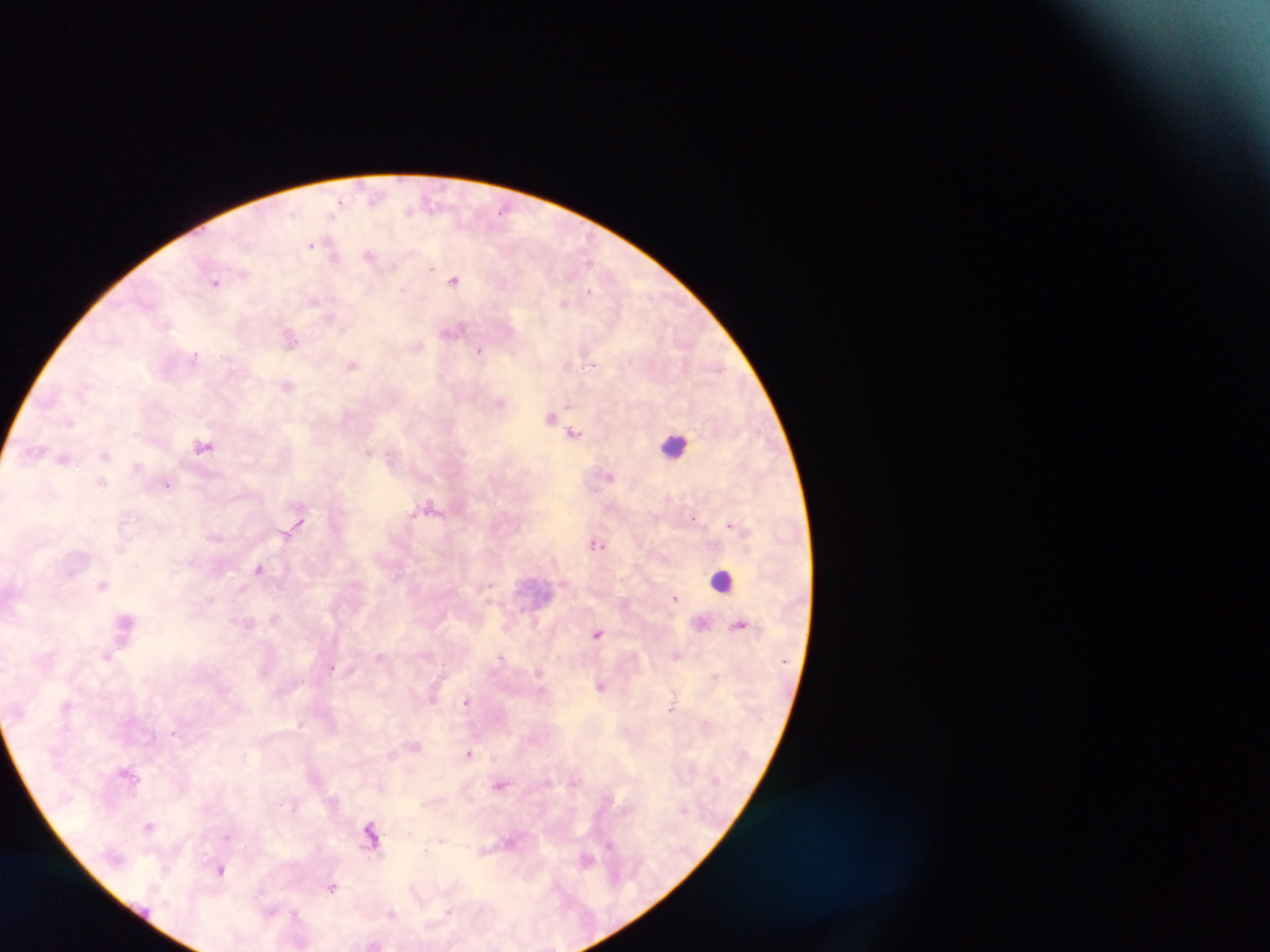
Plasmodium parasite locations = approximate centers as (x, y) in pixels: (295, 210), (410, 210), (501, 210), (330, 218), (311, 245), (370, 255), (333, 257), (588, 262), (431, 269), (453, 280), (216, 282), (402, 288), (589, 289), (564, 303), (329, 320), (290, 338), (419, 345), (481, 350), (195, 353), (567, 365), (593, 365), (351, 366), (287, 385), (499, 402), (568, 403), (551, 417), (575, 433), (202, 447), (369, 450), (105, 455), (391, 457), (139, 465), (610, 477), (101, 482), (168, 484), (432, 504), (302, 517), (695, 519), (731, 526), (286, 532), (597, 544), (258, 567), (103, 585), (488, 586), (677, 598), (273, 618), (125, 623), (740, 624), (598, 634), (380, 655), (675, 655), (107, 656), (502, 657), (332, 670), (600, 686), (433, 698), (467, 701), (67, 704), (672, 708), (302, 724), (175, 734), (414, 744), (469, 753), (126, 772), (574, 780), (501, 784), (334, 801), (294, 809), (369, 824), (148, 826), (370, 830), (228, 835), (441, 839), (610, 843), (371, 845), (425, 851), (151, 852), (587, 859), (219, 870), (331, 888), (416, 889), (270, 910), (449, 910), (296, 912), (391, 914)
image size = 1270×952 pixels
capture = mobile-phone photograph through a microscope
field of view = single
preparation = thick blood film
country = Ghana
leukocyte locations = approximate centers as (x, y) in pixels: (671, 446), (724, 583)